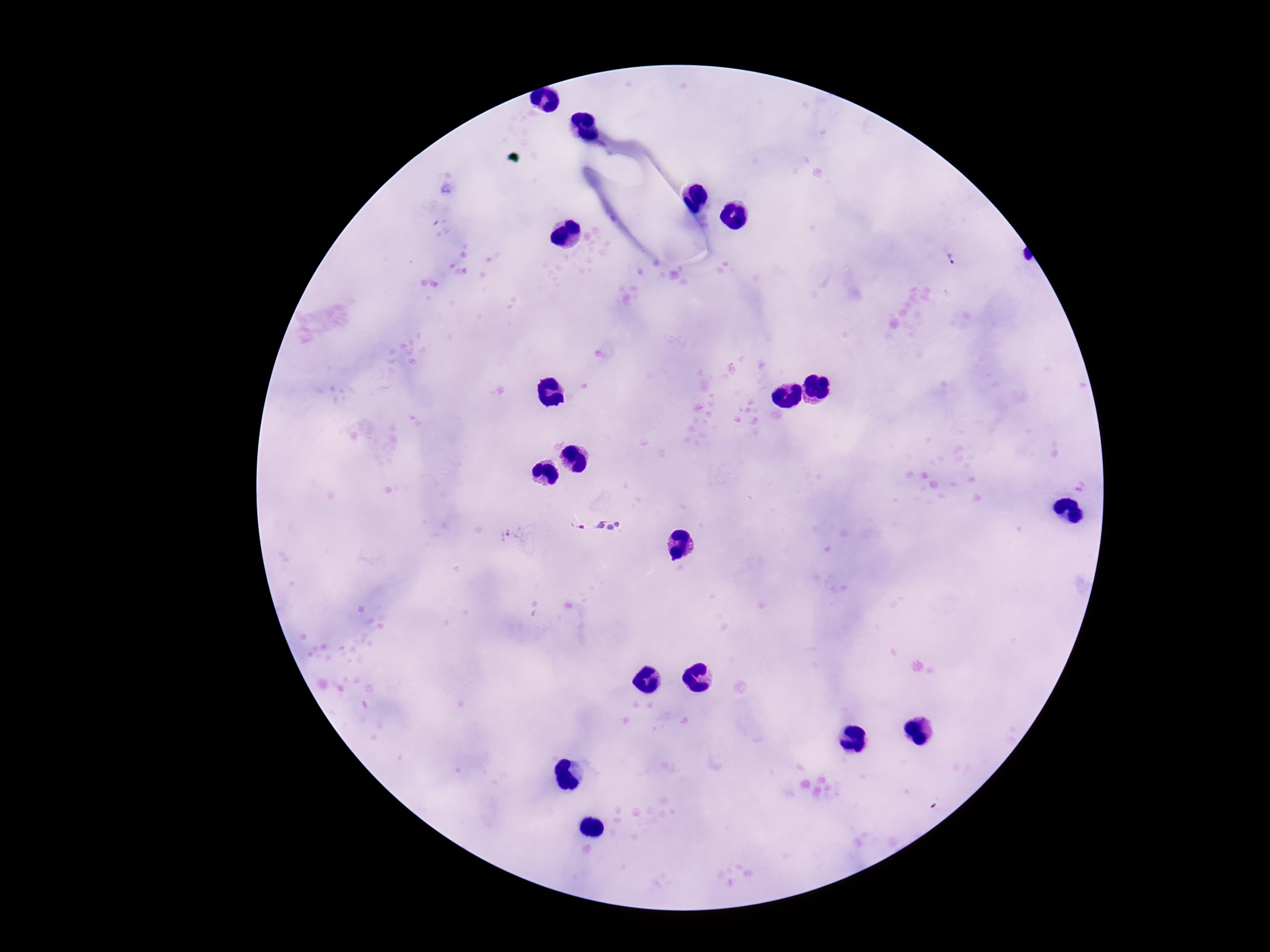

Approximate centers as [x, y] in pixels. Plasmodium parasite locations: [952, 258], [576, 524], [514, 536]. Thick blood film. Photographed through the microscope eyepiece with a smartphone camera. One field from this slide. 100x magnification. Patient malaria status: positive. Giemsa-stained preparation. Image is 1270×952 pixels.